Assess for Plasmodium parasites.
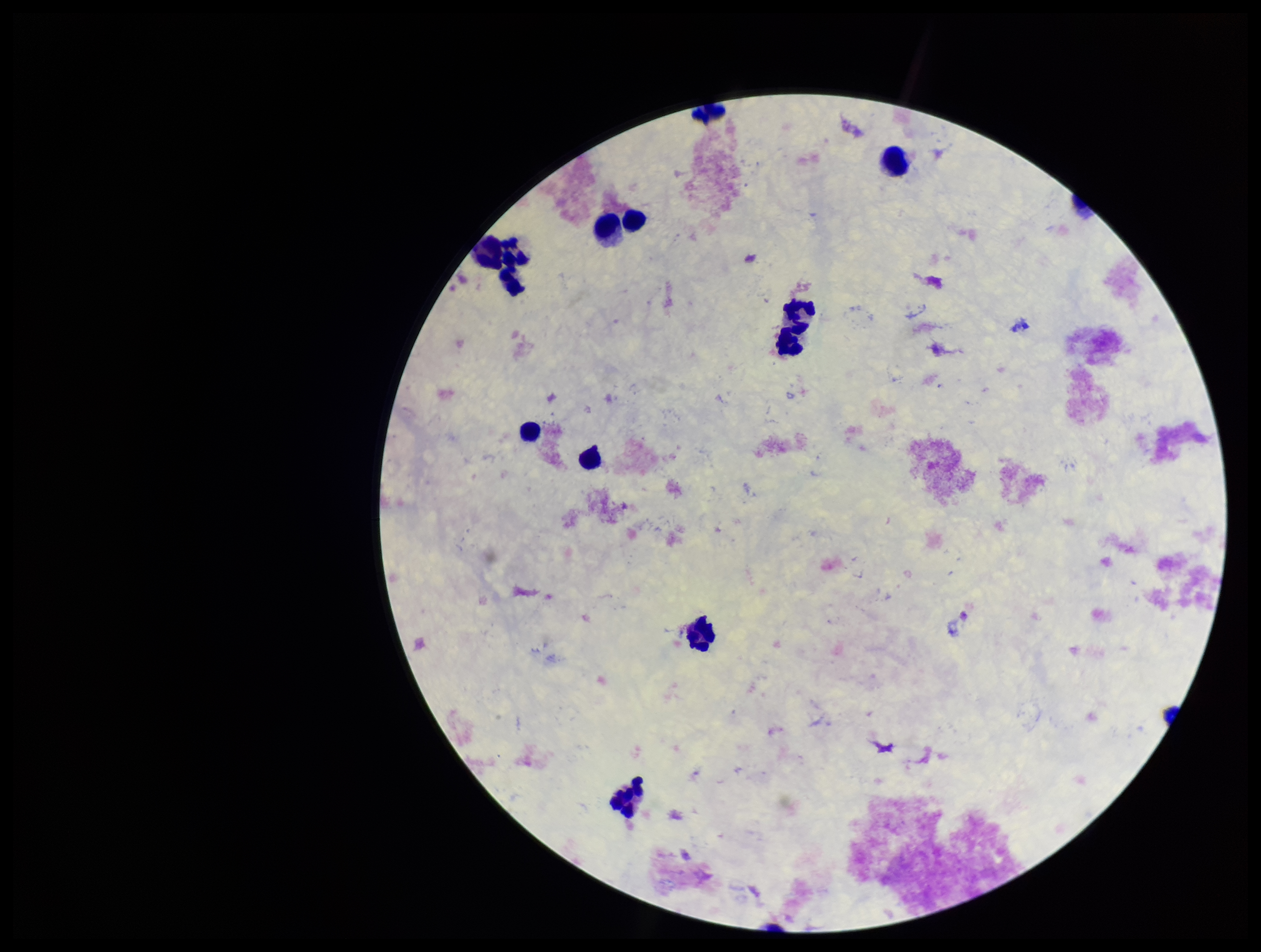

None identified.

{
  "field_of_view": "one from this slide",
  "image_size": "1261×952 pixels",
  "patient_malaria_status": "negative",
  "capture": "smartphone photograph through the microscope eyepiece",
  "stain": "Giemsa",
  "leukocyte_count": 11,
  "parasite_count": 0,
  "preparation": "thick"
}